Assess the morphology of the erythrocytes.
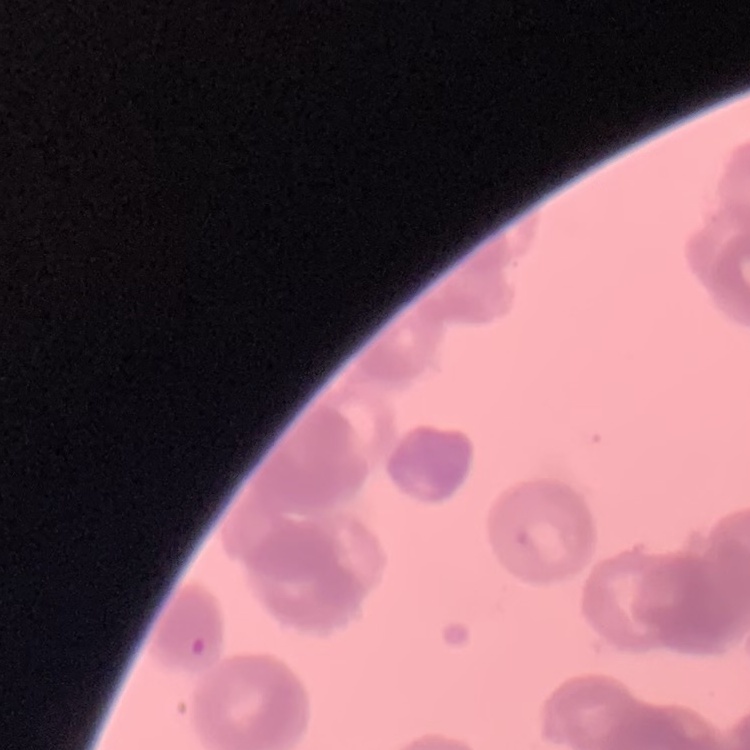

They show rouleaux formation.

image type = square crop of a larger photomicrograph
stain = Field's or Giemsa
preparation = thin blood smear